Locate every blood parasite and identify its species.
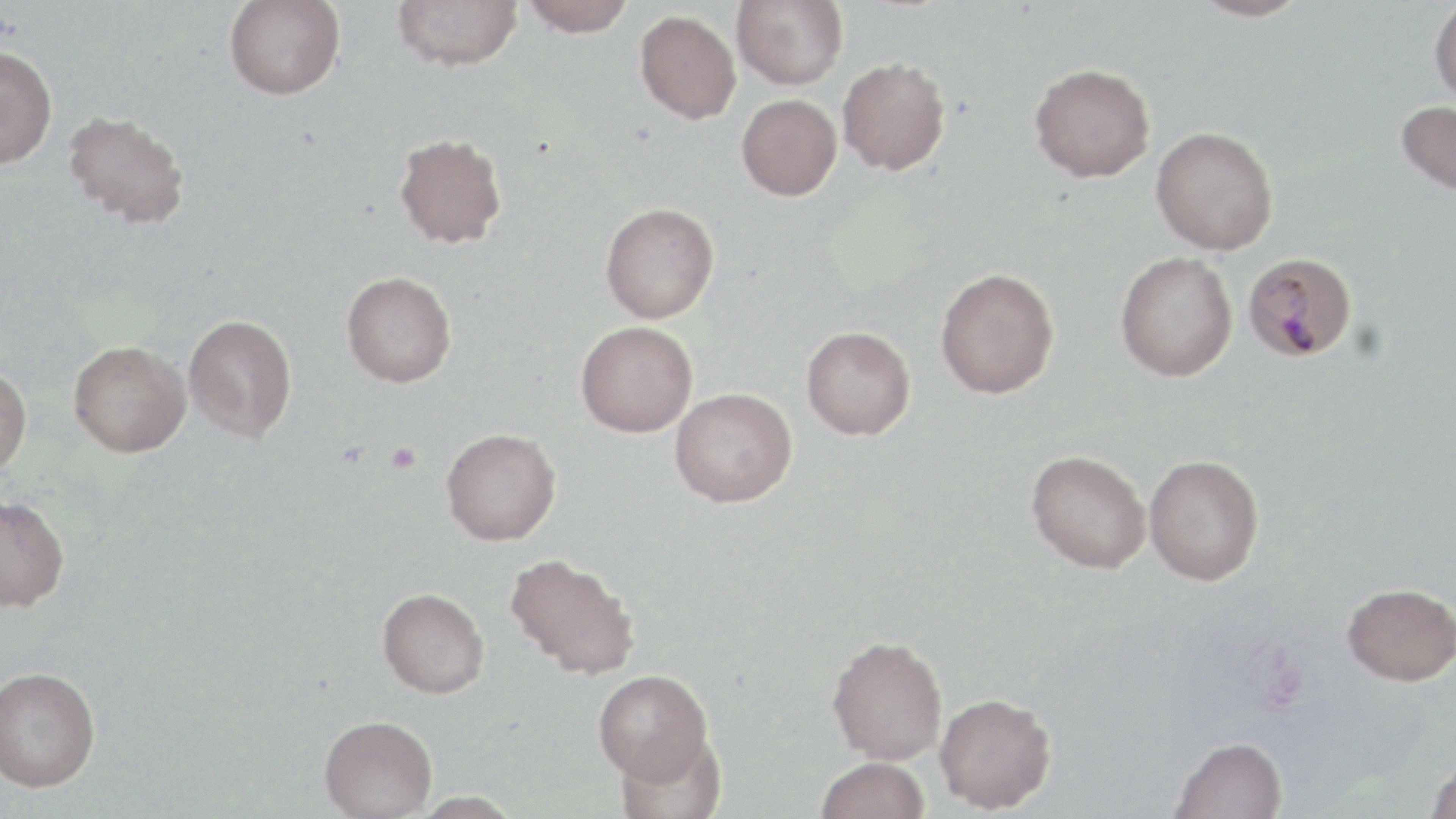

Approximate bounding boxes as (x1,y1)-(x2,y2) corner pairs in pixels.
Plasmodium malariae-infected red blood cells: (1244,252)-(1357,361).
No Plasmodium falciparum, Plasmodium ovale, Plasmodium vivax, Babesia divergens, or Trypanosoma brucei observed.

Platelet locations: (386,443)-(421,475). Uninfected red blood cell locations: (224,0)-(345,100), (392,0)-(522,71), (521,0)-(636,36), (732,0)-(848,90), (1189,0)-(1312,22), (1429,1)-(1456,108), (635,10)-(741,123), (0,45)-(58,168), (837,57)-(950,175), (1029,63)-(1155,182), (736,94)-(842,200), (1396,100)-(1456,196), (64,111)-(190,228), (1151,126)-(1278,255), (394,133)-(507,248), (600,203)-(719,323), (1115,251)-(1238,381), (936,268)-(1059,398), (342,271)-(456,387), (183,314)-(297,442), (576,321)-(697,437), (801,325)-(915,440), (68,340)-(190,457), (0,364)-(31,478), (670,387)-(797,506), (441,428)-(561,545), (1026,449)-(1151,573), (1145,454)-(1264,585), (0,494)-(69,612), (504,552)-(640,679), (1342,582)-(1456,686), (377,587)-(489,698), (827,635)-(947,764), (0,665)-(101,792), (593,669)-(714,784), (935,693)-(1056,812), (319,715)-(437,818), (613,730)-(727,819), (1170,736)-(1288,819), (1425,753)-(1456,819), (815,757)-(930,819), (411,791)-(523,818). Slide-level diagnosis: Plasmodium malariae. Image is 1456×819 pixels. Thin blood film. One field of a larger specimen. Captured at 1000x magnification. May-Grünwald-Giemsa-stained preparation. Light microscopy.